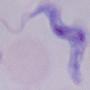

Micrograph. 1000x magnification. A trypanosome is shown.